Classify this cell by malaria status.
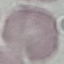

Uninfected.

Thin blood film. Cell patch, automatically extracted from a larger field of view and resized to 64 × 64 pixels. Giemsa stain. Acquired by smartphone through the microscope eyepiece.